Point out malaria parasites and leukocytes.
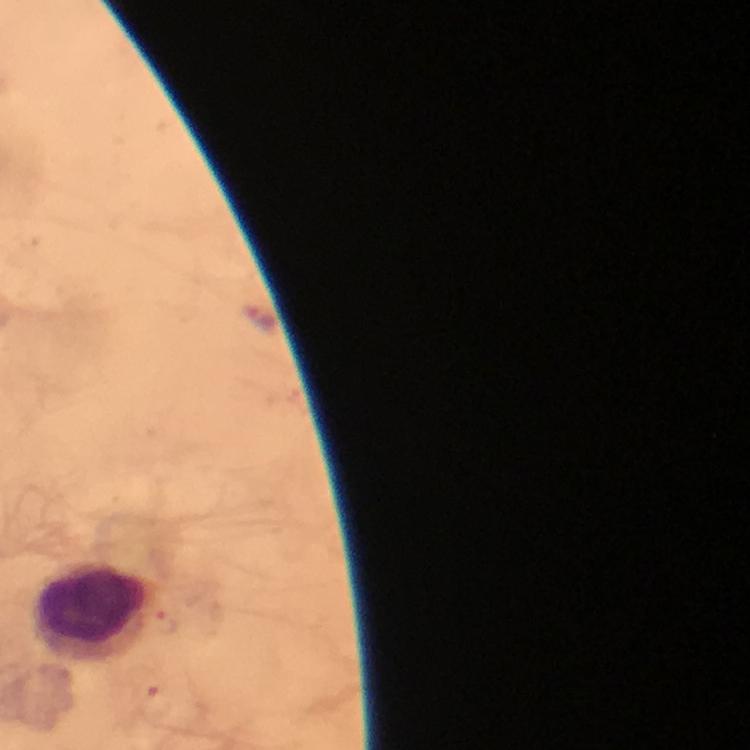
No malaria parasites seen.
Approximate centers as [x, y] in pixels.
Leukocytes: [98, 612].

Immersion oil was used. Giemsa-stained preparation. From a diagnostic examination for malaria. Photographed with a smartphone mounted on the microscope. Thick blood film. 100x magnification. Image is 750×750 pixels. Cropped region of a single field of view.